Identify the preparation type.
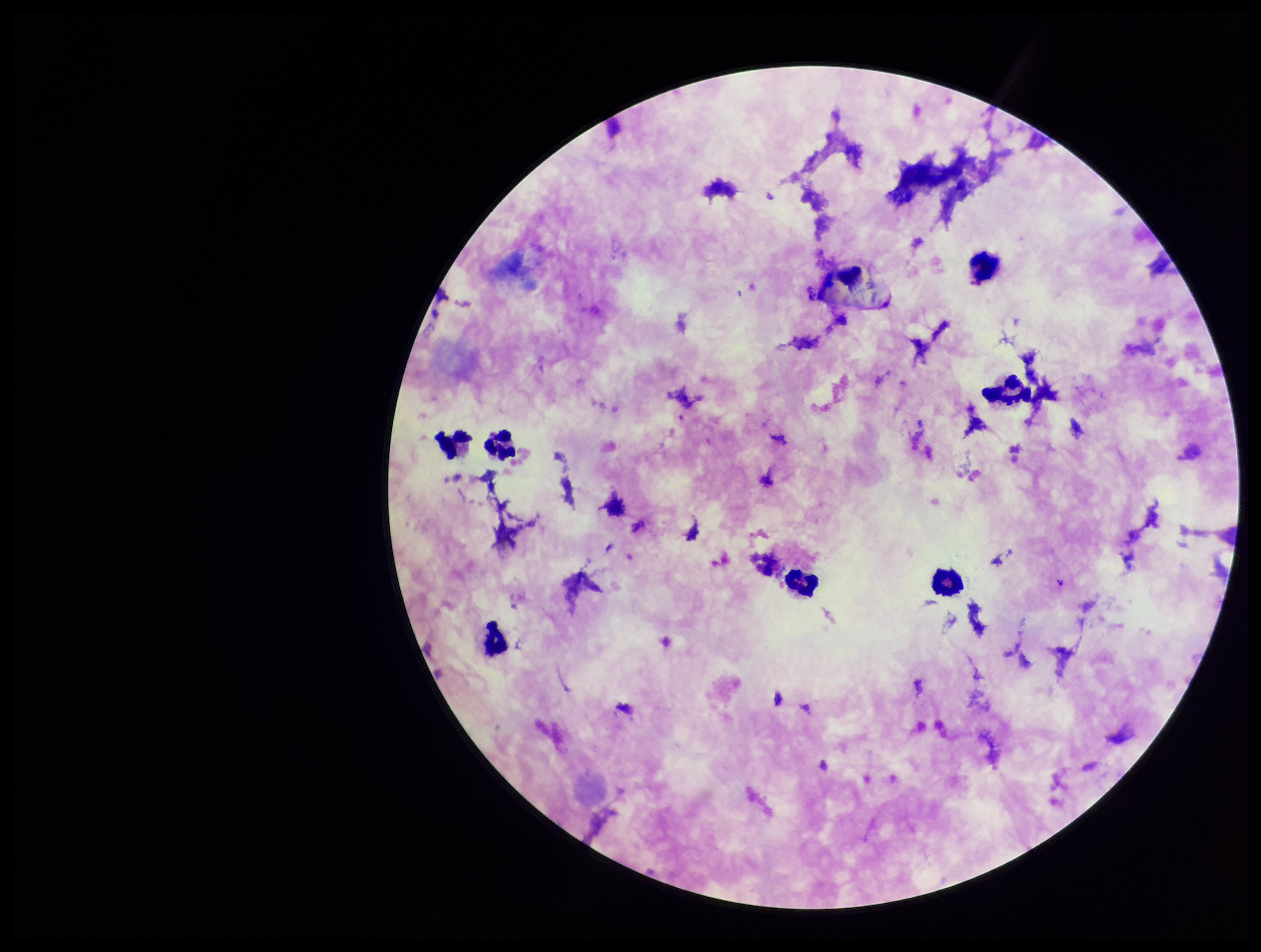
A thick smear.

species reported for this patient = Plasmodium falciparum
parasite count = 0
stain = Giemsa
image size = 1261×952 pixels
patient malaria status = positive
field of view = single
Plasmodium parasites = none detected
capture = smartphone photograph through the microscope eyepiece
leukocyte count = 8